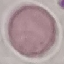
{
  "malaria_status": "uninfected",
  "stain": "Giemsa",
  "preparation": "thin blood film",
  "image_type": "automatically extracted cell patch, resized to 64 × 64 pixels",
  "capture": "smartphone through the microscope eyepiece"
}